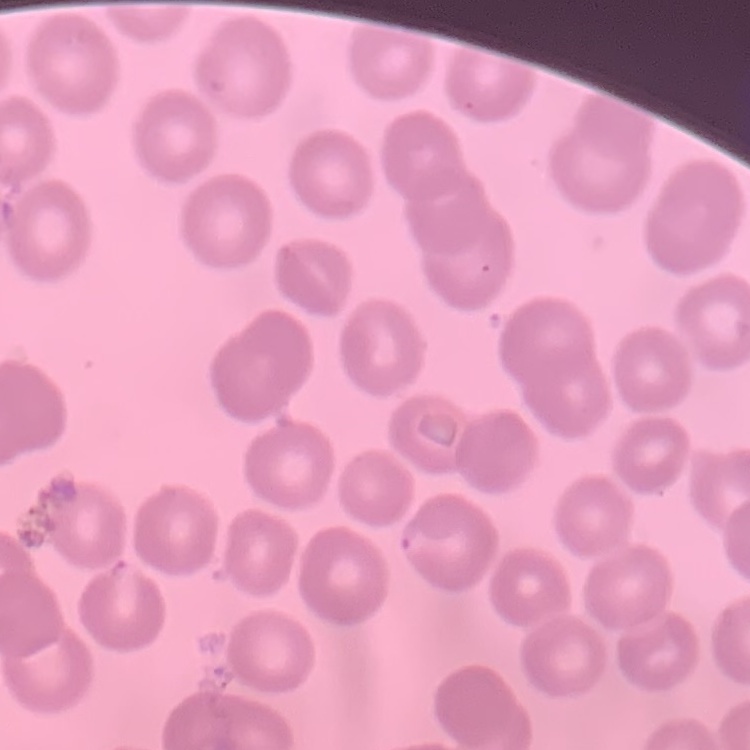 The red blood cells show no rouleaux formation. Square crop of a larger photomicrograph. Field's or Giemsa stain. Thin blood film.